Classify this cell by malaria status.
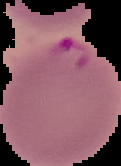
Parasitized.

image type = cell region segmented out of the field of view; surrounding area masked to black
image size = 121×166 pixels
preparation = thin blood smear